Assess this cell for malaria.
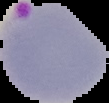
It is parasitized.

Summary:
  - Preparation: thin blood film
  - Image size: 109×103 pixels
  - Image type: segmented cell region on a black background